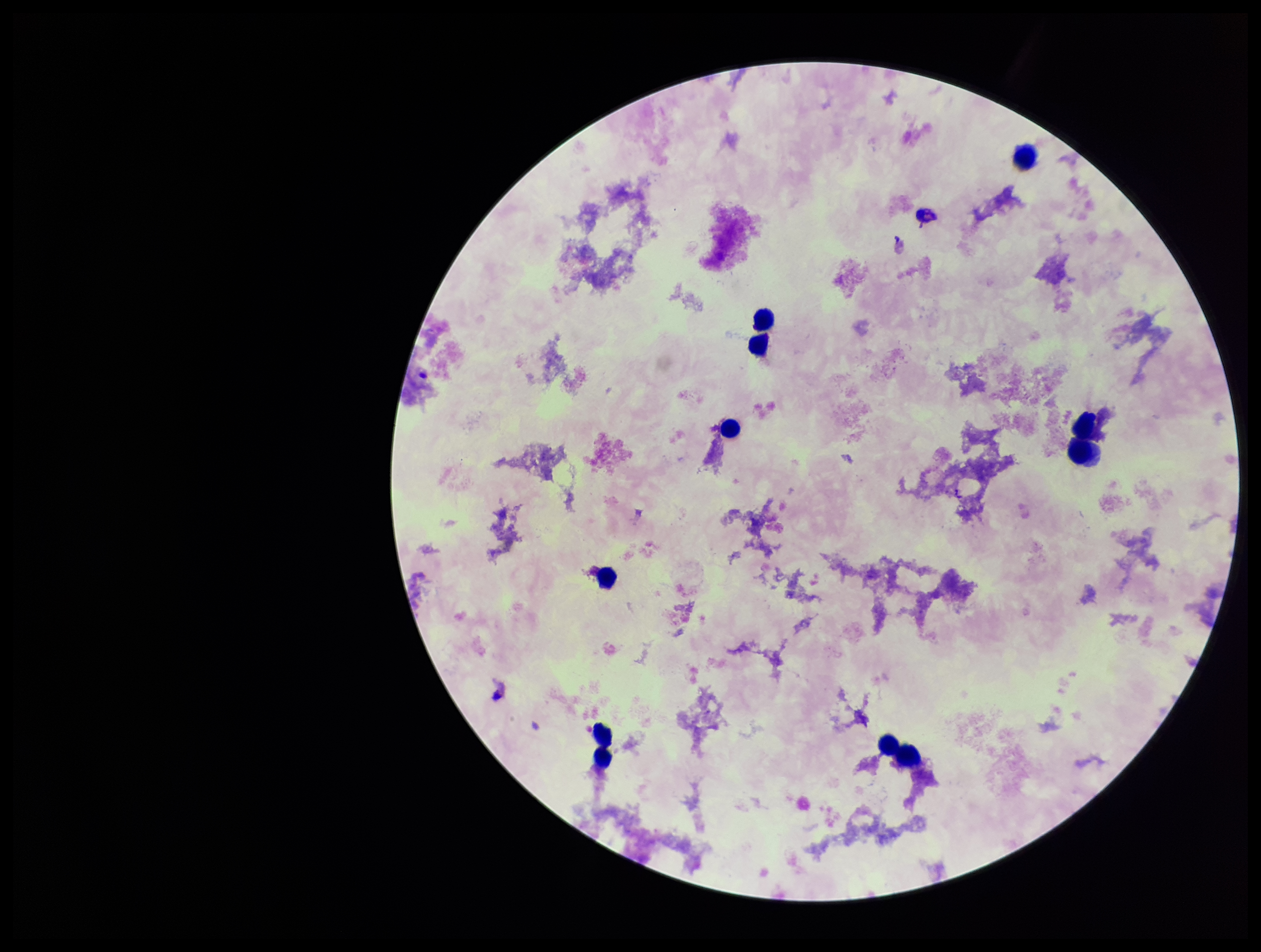
Summary:
  - Plasmodium parasites: none detected
  - Parasite count: 0
  - Leukocyte count: 10
  - Field of view: one from this slide
  - Patient malaria status: negative
  - Capture: smartphone photograph through the microscope eyepiece
  - Stain: Giemsa
  - Preparation: thick smear
  - Image size: 1261×952 pixels